Outline each blood parasite and name the species.
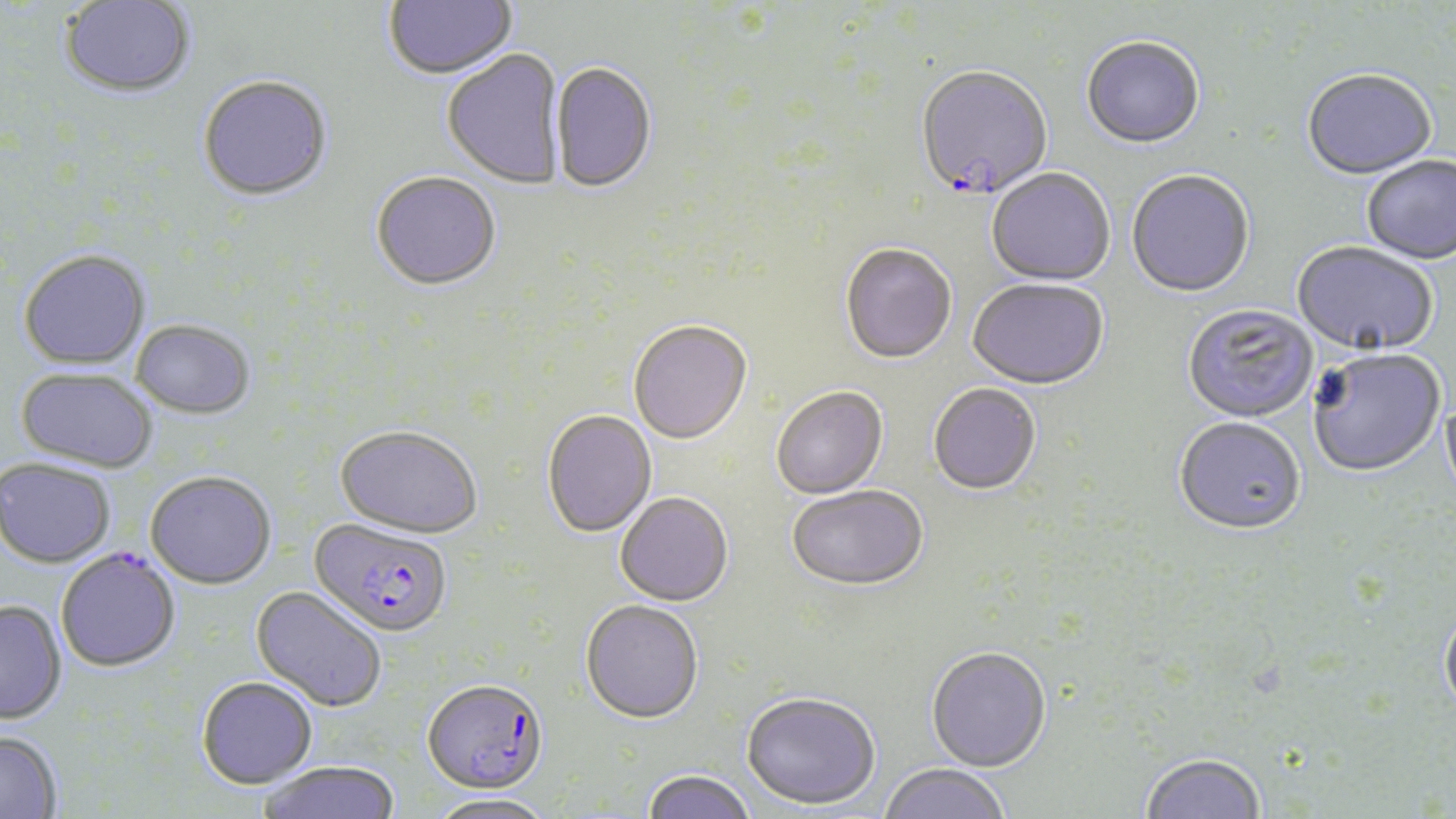
Approximate bounding boxes as named x1/y1/x2/y2 corners in pixels.
Plasmodium falciparum-infected red blood cells: (x1=915, y1=67, x2=1053, y2=203), (x1=309, y1=517, x2=453, y2=636), (x1=56, y1=547, x2=180, y2=671), (x1=421, y1=680, x2=548, y2=798).
No Plasmodium ovale, Plasmodium malariae, Plasmodium vivax, Babesia divergens, or Trypanosoma brucei observed.

{
  "slide_level_diagnosis": "Plasmodium falciparum",
  "modality": "optical microscopy",
  "magnification": "1000x",
  "stain": "May-Grünwald-Giemsa",
  "uninfected_red_blood_cell_locations": "approximate bounding boxes as named x1/y1/x2/y2 corners in pixels: (x1=384, y1=0, x2=518, y2=82), (x1=59, y1=1, x2=196, y2=99), (x1=1081, y1=39, x2=1205, y2=151), (x1=442, y1=51, x2=566, y2=190), (x1=549, y1=63, x2=657, y2=195), (x1=1302, y1=71, x2=1438, y2=183), (x1=197, y1=78, x2=333, y2=203), (x1=1362, y1=157, x2=1456, y2=266), (x1=986, y1=170, x2=1115, y2=288), (x1=1126, y1=171, x2=1255, y2=300), (x1=370, y1=173, x2=501, y2=293), (x1=1292, y1=243, x2=1438, y2=359), (x1=840, y1=245, x2=957, y2=366), (x1=18, y1=249, x2=151, y2=369), (x1=967, y1=281, x2=1108, y2=392), (x1=1182, y1=305, x2=1318, y2=425), (x1=131, y1=319, x2=255, y2=417), (x1=628, y1=322, x2=752, y2=446), (x1=1308, y1=351, x2=1446, y2=480), (x1=15, y1=367, x2=158, y2=473), (x1=928, y1=385, x2=1041, y2=496), (x1=772, y1=388, x2=888, y2=500), (x1=1440, y1=395, x2=1456, y2=507), (x1=542, y1=410, x2=656, y2=537), (x1=1174, y1=419, x2=1305, y2=538), (x1=335, y1=424, x2=483, y2=537), (x1=0, y1=458, x2=116, y2=568), (x1=145, y1=469, x2=277, y2=588), (x1=788, y1=487, x2=929, y2=593), (x1=615, y1=492, x2=733, y2=606), (x1=251, y1=586, x2=388, y2=712), (x1=580, y1=599, x2=704, y2=723), (x1=0, y1=600, x2=66, y2=724), (x1=1439, y1=608, x2=1456, y2=721), (x1=926, y1=649, x2=1052, y2=774), (x1=196, y1=676, x2=318, y2=788), (x1=741, y1=693, x2=880, y2=811), (x1=0, y1=730, x2=62, y2=819), (x1=1140, y1=755, x2=1266, y2=819), (x1=257, y1=760, x2=401, y2=819), (x1=879, y1=764, x2=1010, y2=819), (x1=642, y1=769, x2=757, y2=819), (x1=428, y1=792, x2=556, y2=819)",
  "image_size": "1456×819 pixels",
  "preparation": "thin blood film",
  "field_of_view": "one of a larger specimen"
}